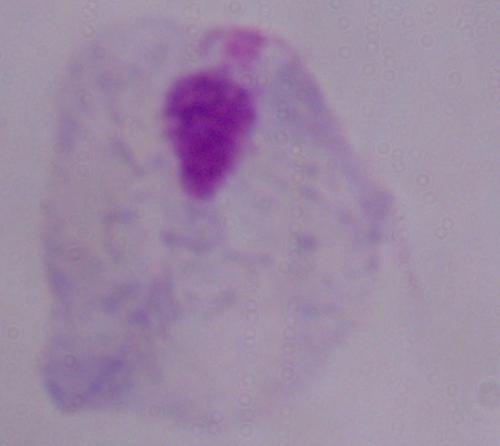

Summary:
  - Modality: photomicrograph
  - Magnification: 1000x
  - Identification: trichomonad